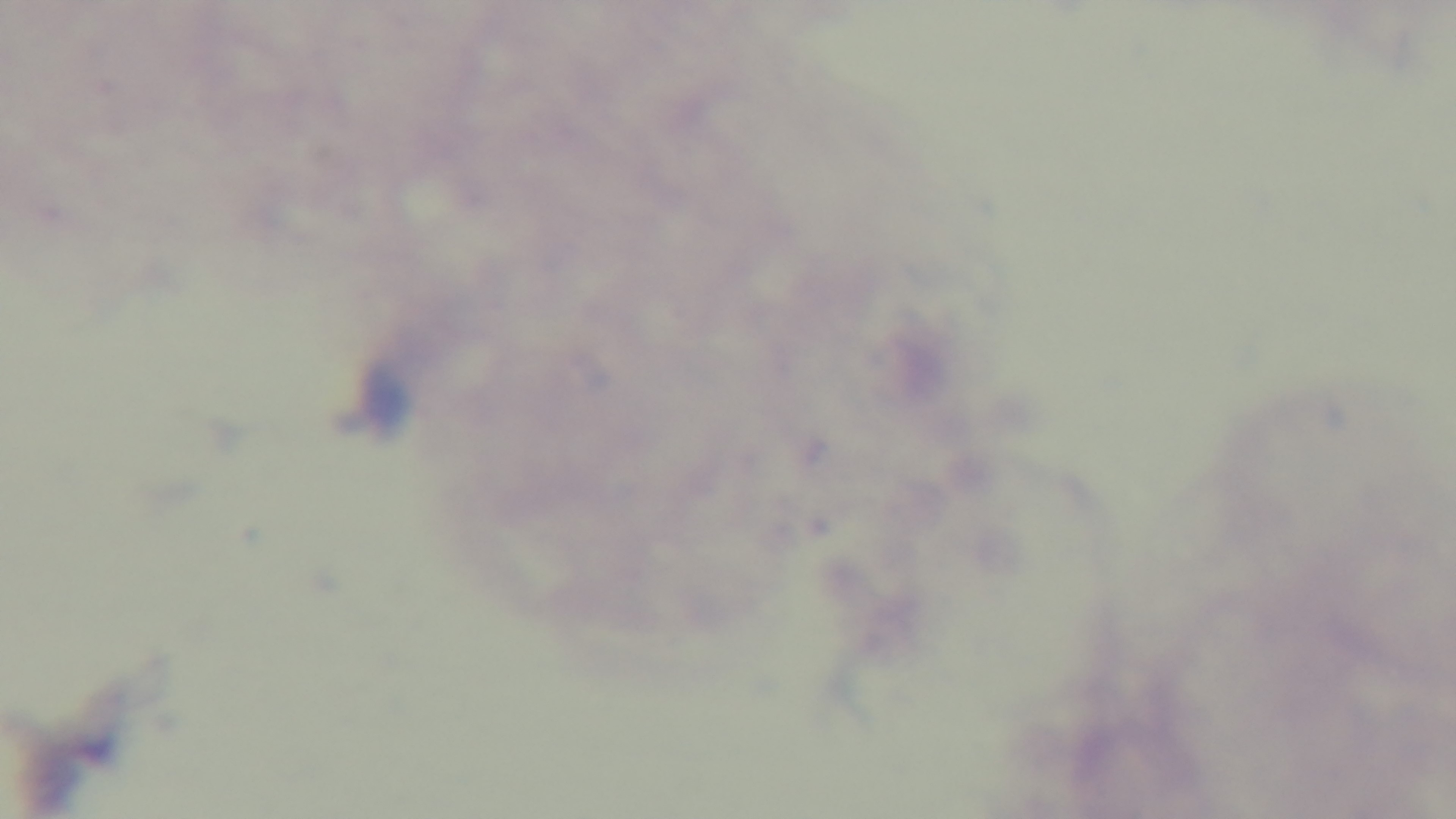

field of view = one from the slide
objective = 100x oil immersion
capture = mounted 4K digital camera
malaria status = uninfected
preparation = thick
modality = light microscopy
stain = Giemsa